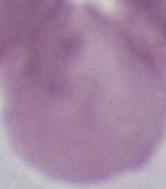

identification = red blood cell
modality = micrograph
magnification = 1000x